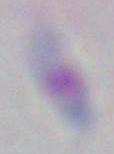
Captured at 1000x magnification. Photomicrograph. Toxoplasma gondii is shown.